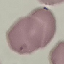
result: no malaria parasites seen
image_type: cell patch, automatically extracted from a larger field of view and resized to 64 × 64 pixels
stain: Giemsa
preparation: thin blood smear
capture: smartphone camera at the microscope eyepiece